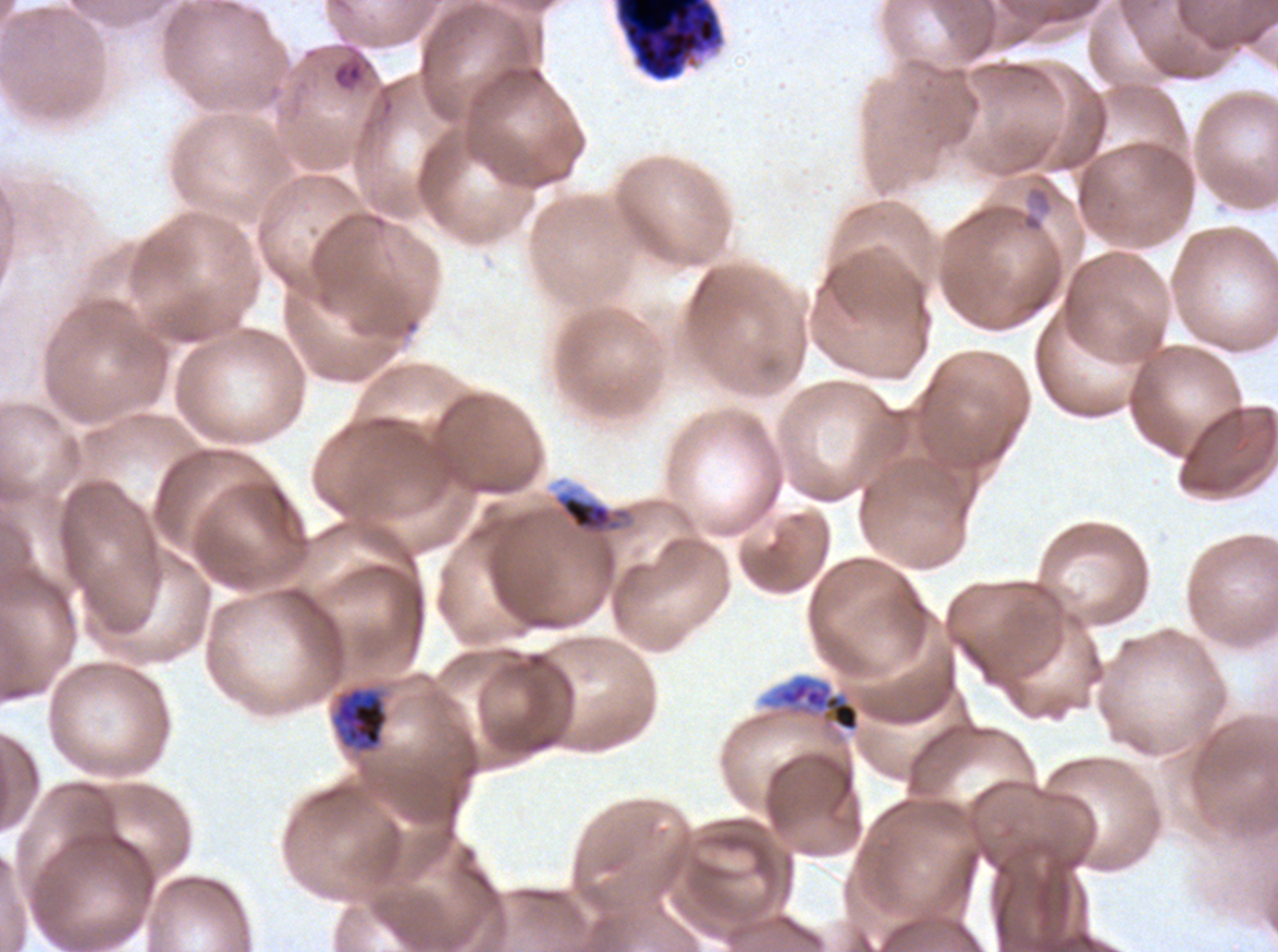

Approximate bounding boxes as {x1, y1, x2, y2} in pixels. Debris locations: {613, 0, 725, 82}, {553, 490, 633, 538}. Early schizont locations: {769, 674, 861, 733}. Late trophozoite locations: {335, 688, 388, 751}. Late-ring/early-trophozoite locations: {332, 60, 364, 90}. P. falciparum cultured ex vivo for 24 to 48 hours, from a patient in The Gambia. Image is 1278×952 pixels. Thin blood smear. One sub-image of a larger composite. Life-cycle stages observed: late-ring/early-trophozoite, late trophozoite, early schizont. Giemsa stain.